Identify the blood parasite species.
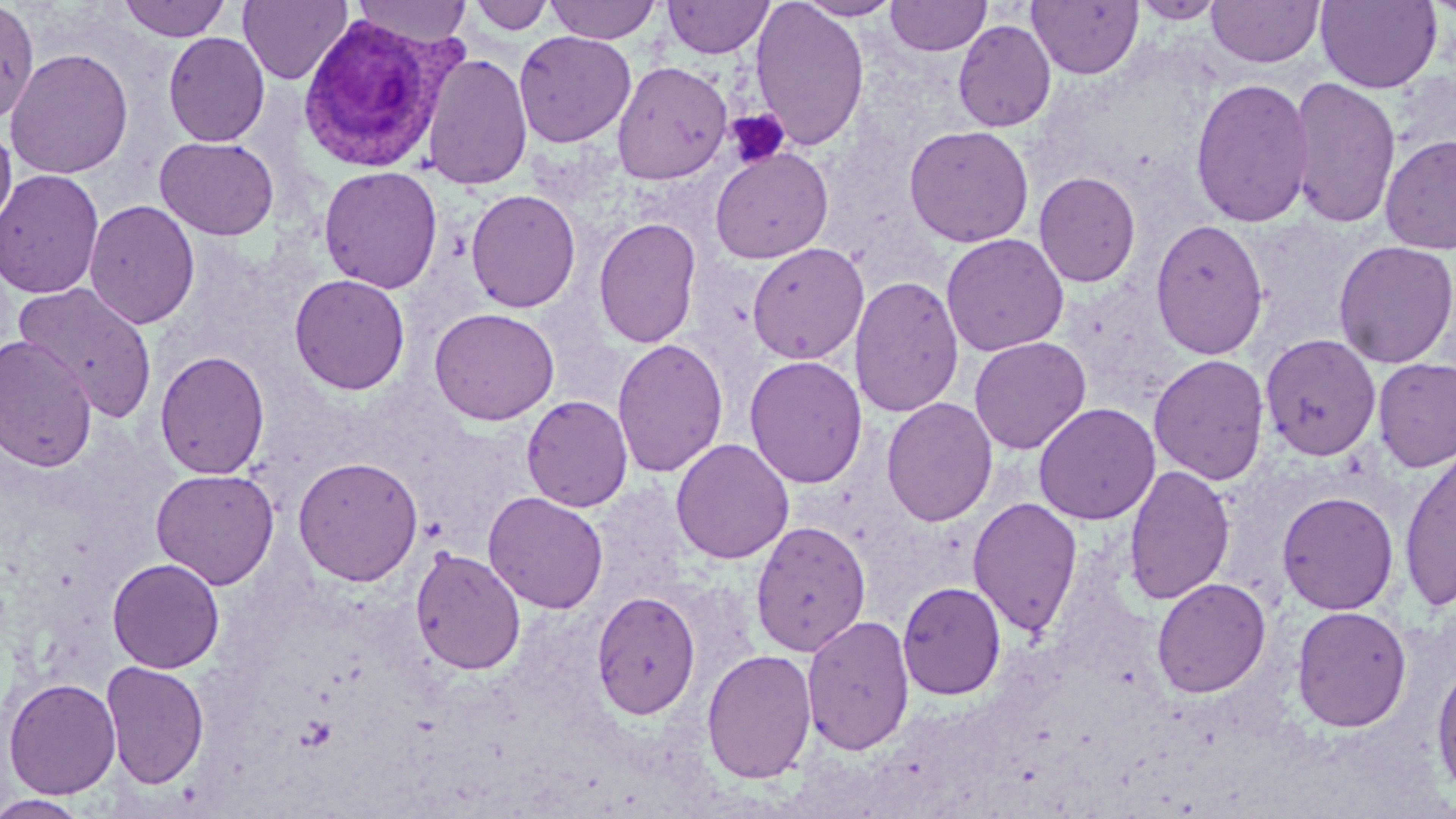

Plasmodium vivax.

Approximate bounding boxes as named x1/y1/x2/y2 corners in pixels. Platelet locations: (x1=725, y1=109, x2=792, y2=169). Plasmodium vivax-infected red blood cell locations: (x1=297, y1=13, x2=452, y2=173). Uninfected red blood cell locations: (x1=118, y1=0, x2=232, y2=41), (x1=238, y1=0, x2=351, y2=85), (x1=351, y1=0, x2=473, y2=48), (x1=544, y1=0, x2=662, y2=44), (x1=749, y1=0, x2=870, y2=151), (x1=795, y1=0, x2=904, y2=21), (x1=885, y1=0, x2=991, y2=56), (x1=1131, y1=0, x2=1228, y2=24), (x1=1315, y1=0, x2=1443, y2=93), (x1=467, y1=1, x2=556, y2=35), (x1=662, y1=1, x2=774, y2=59), (x1=1028, y1=1, x2=1143, y2=79), (x1=1206, y1=1, x2=1324, y2=67), (x1=0, y1=3, x2=39, y2=125), (x1=952, y1=20, x2=1057, y2=133), (x1=514, y1=30, x2=636, y2=147), (x1=163, y1=32, x2=270, y2=147), (x1=5, y1=48, x2=134, y2=179), (x1=422, y1=52, x2=533, y2=190), (x1=612, y1=60, x2=733, y2=184), (x1=1287, y1=76, x2=1402, y2=229), (x1=1189, y1=77, x2=1314, y2=228), (x1=0, y1=120, x2=17, y2=236), (x1=903, y1=124, x2=1035, y2=248), (x1=1379, y1=133, x2=1456, y2=255), (x1=154, y1=136, x2=280, y2=240), (x1=710, y1=147, x2=834, y2=264), (x1=318, y1=165, x2=443, y2=294), (x1=0, y1=168, x2=104, y2=299), (x1=1033, y1=171, x2=1141, y2=288), (x1=465, y1=189, x2=581, y2=313), (x1=84, y1=200, x2=200, y2=330), (x1=593, y1=217, x2=702, y2=348), (x1=1150, y1=217, x2=1269, y2=360), (x1=940, y1=233, x2=1069, y2=356), (x1=1333, y1=240, x2=1456, y2=368), (x1=747, y1=243, x2=869, y2=364), (x1=289, y1=273, x2=410, y2=395), (x1=850, y1=275, x2=965, y2=419), (x1=14, y1=282, x2=158, y2=421), (x1=429, y1=307, x2=560, y2=426), (x1=1260, y1=334, x2=1381, y2=460), (x1=0, y1=335, x2=97, y2=473), (x1=969, y1=336, x2=1091, y2=454), (x1=612, y1=337, x2=728, y2=477), (x1=154, y1=350, x2=270, y2=480), (x1=1148, y1=353, x2=1270, y2=486), (x1=744, y1=355, x2=868, y2=488), (x1=1372, y1=357, x2=1456, y2=472), (x1=521, y1=395, x2=633, y2=512), (x1=881, y1=397, x2=998, y2=526), (x1=1033, y1=402, x2=1160, y2=525), (x1=670, y1=437, x2=794, y2=564), (x1=1400, y1=447, x2=1455, y2=612), (x1=292, y1=456, x2=424, y2=586), (x1=1122, y1=464, x2=1235, y2=604), (x1=151, y1=468, x2=279, y2=589), (x1=483, y1=490, x2=609, y2=614), (x1=1276, y1=490, x2=1400, y2=615), (x1=967, y1=496, x2=1083, y2=636), (x1=749, y1=520, x2=871, y2=657), (x1=410, y1=546, x2=527, y2=675), (x1=107, y1=557, x2=225, y2=674), (x1=1151, y1=578, x2=1272, y2=698), (x1=897, y1=581, x2=1007, y2=700), (x1=590, y1=590, x2=701, y2=720), (x1=1291, y1=605, x2=1412, y2=732), (x1=801, y1=614, x2=915, y2=755), (x1=701, y1=648, x2=817, y2=784), (x1=100, y1=659, x2=209, y2=789), (x1=1431, y1=659, x2=1456, y2=800), (x1=3, y1=677, x2=121, y2=799), (x1=0, y1=794, x2=92, y2=819). Thin blood smear. One field of a larger specimen. Captured at 1000x magnification. May-Grünwald-Giemsa-stained preparation. Light microscopy. Image is 1456×819 pixels.